Locate every Plasmodium parasite.
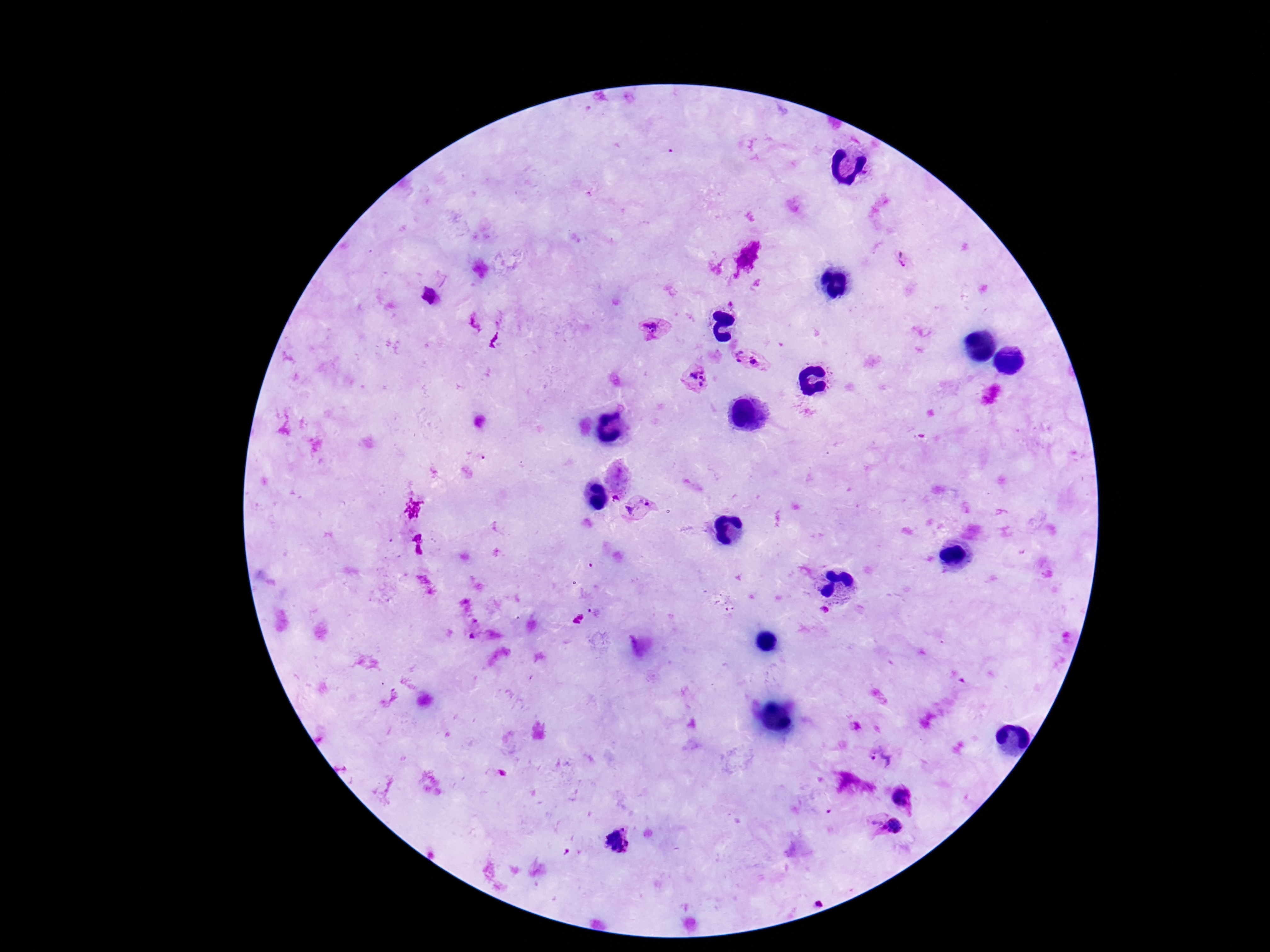

Approximate centers as {x, y} in pixels.
Plasmodium parasites: {429, 294}, {651, 328}, {739, 351}, {754, 360}, {739, 361}, {699, 377}, {615, 498}, {648, 504}, {631, 507}, {880, 758}, {900, 796}, {876, 823}, {895, 826}, {615, 840}, {818, 904}.

Summary:
  - Stain: Giemsa
  - Capture: smartphone camera through the microscope eyepiece
  - Field of view: one from this slide
  - Magnification: 100x
  - Patient malaria status: infected
  - Preparation: thick blood film
  - Image size: 1270×952 pixels